Name the cell type shown.
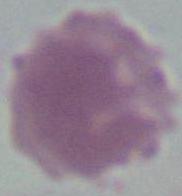

An erythrocyte.

Micrograph. Captured at 1000x magnification.